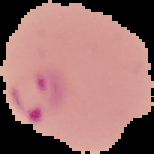

From a thin blood smear. Malaria status: parasitized. Cell region segmented out of the field of view; the surrounding area is masked to black. Image is 154×154 pixels.